Report the malaria status of this cell.
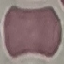

Uninfected.

Giemsa-stained preparation. Photographed with a smartphone camera at the microscope eyepiece. Automatically extracted cell patch, resized to 64 × 64 pixels. Thin blood smear.